Report the malaria status of this cell.
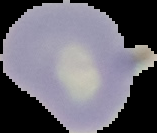

It is uninfected.

Image is 157×133 pixels. Cell region segmented out of the field of view; the surrounding area is masked to black. From a thin blood film.